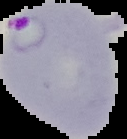
Malaria status: parasitized. Segmented cell region on a black background. From a thin blood film. Image is 127×139 pixels.